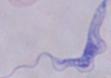
Summary:
  - Magnification: 1000x
  - Modality: photomicrograph
  - Identification: trypanosome